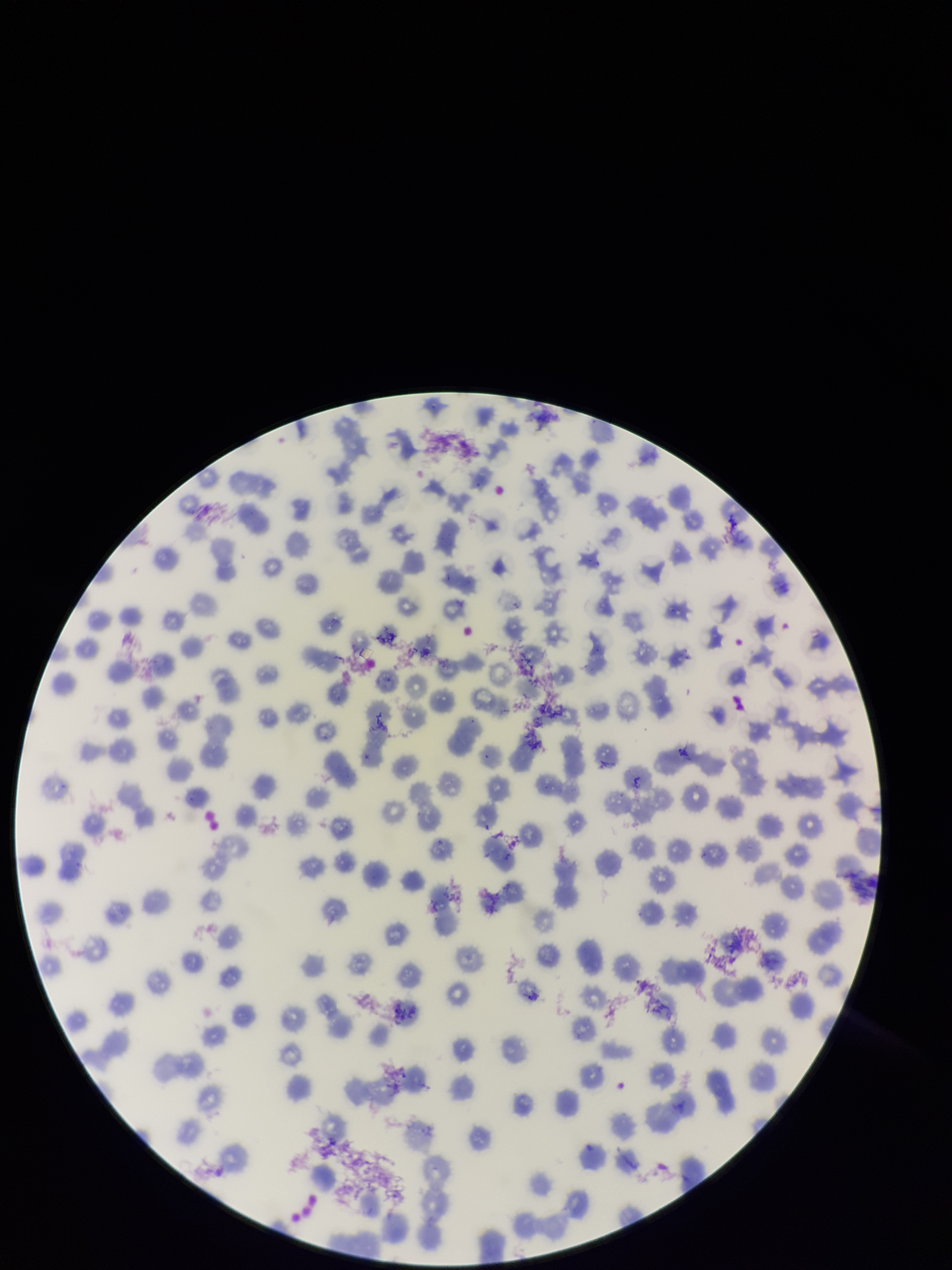

Summary:
  - Stain: Giemsa
  - Field of view: one from this slide
  - Preparation: thin smear
  - Parasitized red blood cell count: 0
  - Patient malaria status: negative
  - Capture: smartphone photograph through the microscope eyepiece
  - Parasitized red blood cells: none identified
  - Red blood cell count: 248
  - Image size: 952×1270 pixels